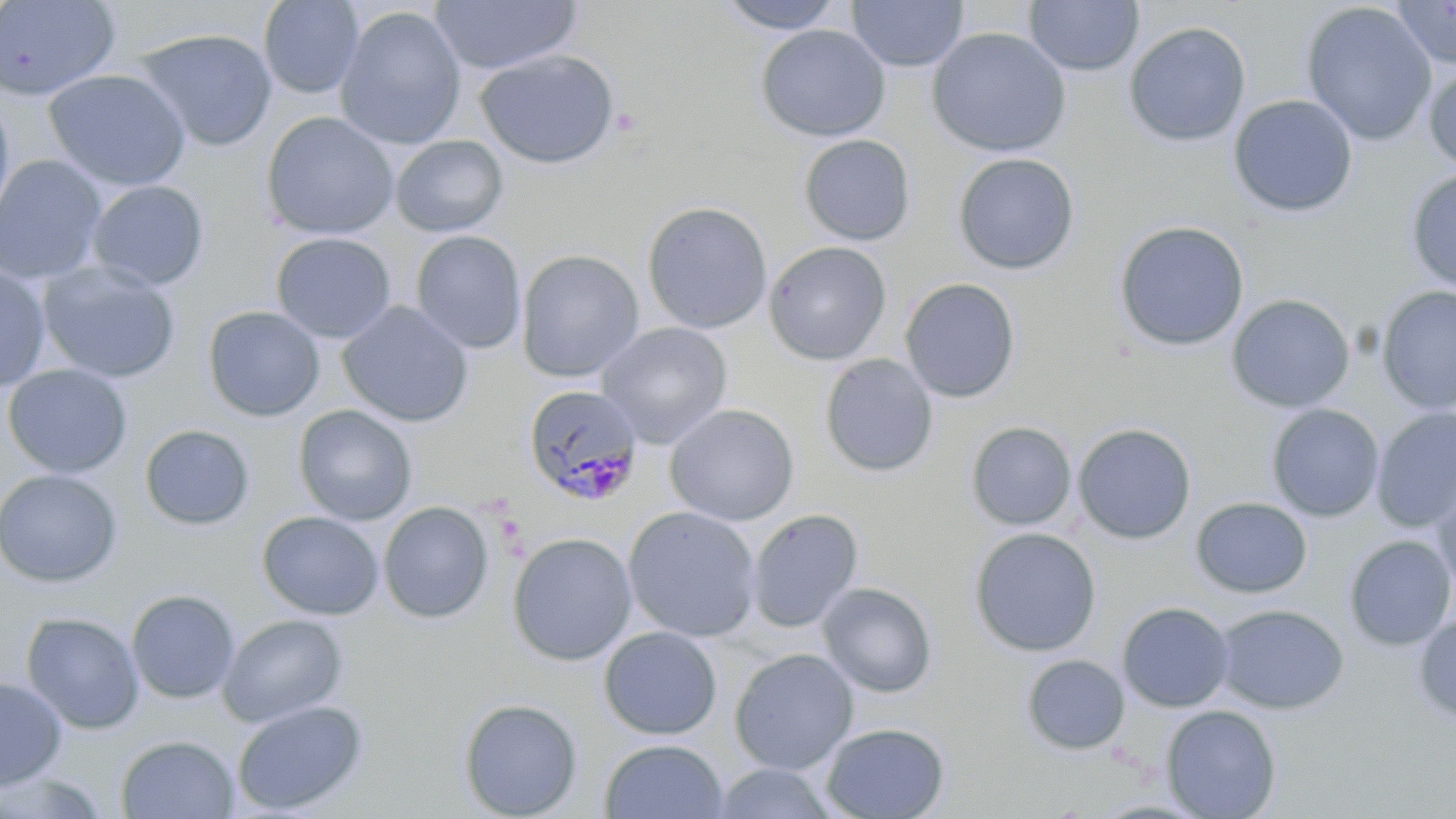

Summary:
  - Coordinate format: approximate bounding boxes as named x1/y1/x2/y2 corners in pixels
  - Uninfected red blood cell locations: (x1=0, y1=0, x2=122, y2=101), (x1=258, y1=0, x2=365, y2=99), (x1=429, y1=0, x2=582, y2=76), (x1=716, y1=0, x2=847, y2=34), (x1=846, y1=0, x2=969, y2=72), (x1=1023, y1=0, x2=1143, y2=77), (x1=1390, y1=0, x2=1456, y2=69), (x1=1299, y1=2, x2=1437, y2=146), (x1=334, y1=6, x2=467, y2=150), (x1=1123, y1=21, x2=1251, y2=148), (x1=755, y1=24, x2=891, y2=142), (x1=135, y1=27, x2=278, y2=153), (x1=926, y1=27, x2=1072, y2=158), (x1=475, y1=49, x2=620, y2=169), (x1=1423, y1=62, x2=1456, y2=174), (x1=44, y1=68, x2=191, y2=191), (x1=0, y1=93, x2=16, y2=231), (x1=1228, y1=94, x2=1359, y2=218), (x1=260, y1=111, x2=399, y2=241), (x1=390, y1=134, x2=509, y2=238), (x1=797, y1=134, x2=916, y2=247), (x1=952, y1=152, x2=1080, y2=274), (x1=0, y1=155, x2=108, y2=284), (x1=1404, y1=168, x2=1456, y2=295), (x1=86, y1=180, x2=210, y2=290), (x1=642, y1=201, x2=773, y2=334), (x1=1113, y1=220, x2=1250, y2=352), (x1=411, y1=231, x2=527, y2=354), (x1=270, y1=232, x2=396, y2=344), (x1=763, y1=241, x2=892, y2=366), (x1=516, y1=250, x2=645, y2=382), (x1=37, y1=261, x2=181, y2=383), (x1=0, y1=265, x2=52, y2=394), (x1=899, y1=277, x2=1021, y2=403), (x1=1375, y1=285, x2=1456, y2=414), (x1=1226, y1=293, x2=1356, y2=413), (x1=337, y1=301, x2=475, y2=428), (x1=202, y1=305, x2=325, y2=422), (x1=596, y1=321, x2=733, y2=448), (x1=819, y1=353, x2=939, y2=478), (x1=2, y1=364, x2=133, y2=479), (x1=1266, y1=403, x2=1384, y2=522), (x1=664, y1=404, x2=800, y2=526), (x1=293, y1=405, x2=417, y2=526), (x1=1371, y1=407, x2=1456, y2=532), (x1=965, y1=421, x2=1078, y2=531), (x1=1072, y1=423, x2=1197, y2=544), (x1=139, y1=424, x2=254, y2=531), (x1=0, y1=468, x2=123, y2=588), (x1=1430, y1=478, x2=1456, y2=597), (x1=1191, y1=497, x2=1312, y2=599), (x1=377, y1=501, x2=494, y2=624), (x1=622, y1=506, x2=762, y2=642), (x1=746, y1=509, x2=864, y2=633), (x1=257, y1=511, x2=384, y2=620), (x1=968, y1=527, x2=1102, y2=657), (x1=506, y1=532, x2=637, y2=666), (x1=1343, y1=534, x2=1456, y2=651), (x1=817, y1=582, x2=938, y2=698), (x1=126, y1=589, x2=241, y2=704), (x1=1116, y1=601, x2=1235, y2=712), (x1=1214, y1=604, x2=1348, y2=714), (x1=20, y1=612, x2=145, y2=734), (x1=1413, y1=612, x2=1456, y2=725), (x1=218, y1=613, x2=348, y2=728), (x1=598, y1=626, x2=722, y2=740), (x1=729, y1=648, x2=859, y2=775), (x1=1021, y1=653, x2=1130, y2=756), (x1=0, y1=676, x2=68, y2=790), (x1=458, y1=697, x2=583, y2=818), (x1=231, y1=699, x2=369, y2=815), (x1=1160, y1=705, x2=1282, y2=819), (x1=820, y1=722, x2=950, y2=819), (x1=115, y1=734, x2=240, y2=818), (x1=599, y1=738, x2=728, y2=819), (x1=710, y1=762, x2=841, y2=818), (x1=1, y1=769, x2=111, y2=817)
  - Plasmodium malariae-infected red blood cell locations: (x1=522, y1=383, x2=645, y2=507)
  - Slide-level diagnosis: Plasmodium malariae
  - Magnification: 1000x
  - Field of view: one of a larger specimen
  - Image size: 1456×819 pixels
  - Modality: light microscopy
  - Preparation: thin blood smear
  - Stain: May-Grünwald-Giemsa